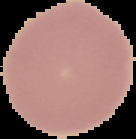

Summary:
  - Image size: 136×139 pixels
  - Image type: cell region segmented out of the field of view; surrounding area masked to black
  - Preparation: thin blood smear
  - Malaria status: uninfected